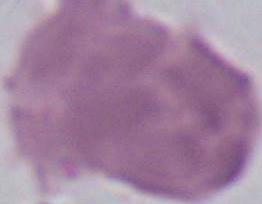
Summary:
  - Magnification: 1000x
  - Modality: micrograph
  - Identification: red blood cell